Classify this cell by malaria status.
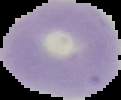
Uninfected.

From a thin blood film. The area outside the segmented cell region is set to black. Image is 121×100 pixels.